Assess this cell for malaria.
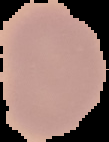
It is uninfected.

From a thin blood smear. The area outside the segmented cell region is set to black. Image is 109×142 pixels.